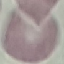

Summary:
  - Result: negative for malaria parasites
  - Preparation: thin blood film
  - Capture: smartphone camera at the microscope eyepiece
  - Stain: Giemsa
  - Image type: cell patch, automatically extracted from a larger field of view and resized to 64 × 64 pixels